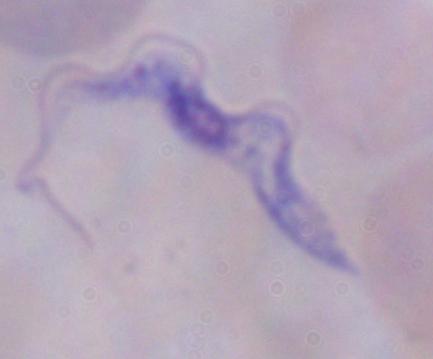

Summary:
  - Identification: trypanosome
  - Magnification: 1000x
  - Modality: micrograph